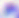 Photomicrograph. Toxoplasma gondii is shown. Captured at 400x magnification.